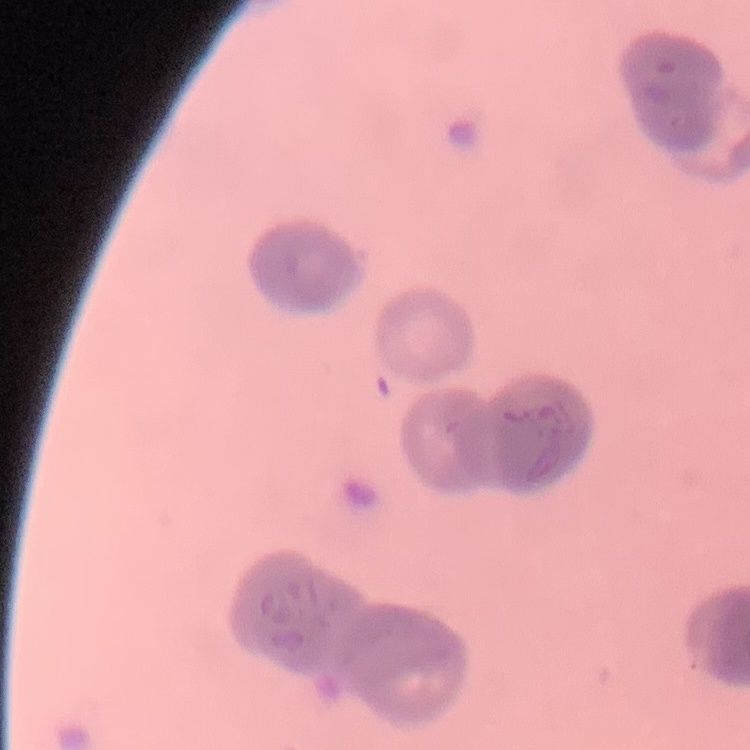

erythrocyte morphology = rouleaux formation
preparation = thin blood film
stain = Field's or Giemsa
image type = one tile cut from a larger photomicrograph